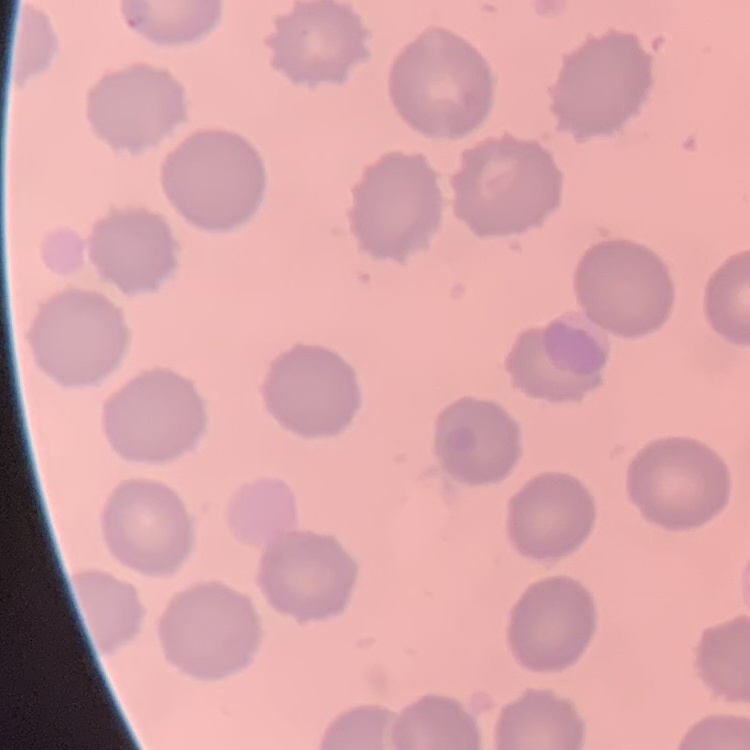

The erythrocytes exhibit no rouleaux formation. One tile cut from a larger photomicrograph. Stained with either Field's or Giemsa. Thin peripheral smear.